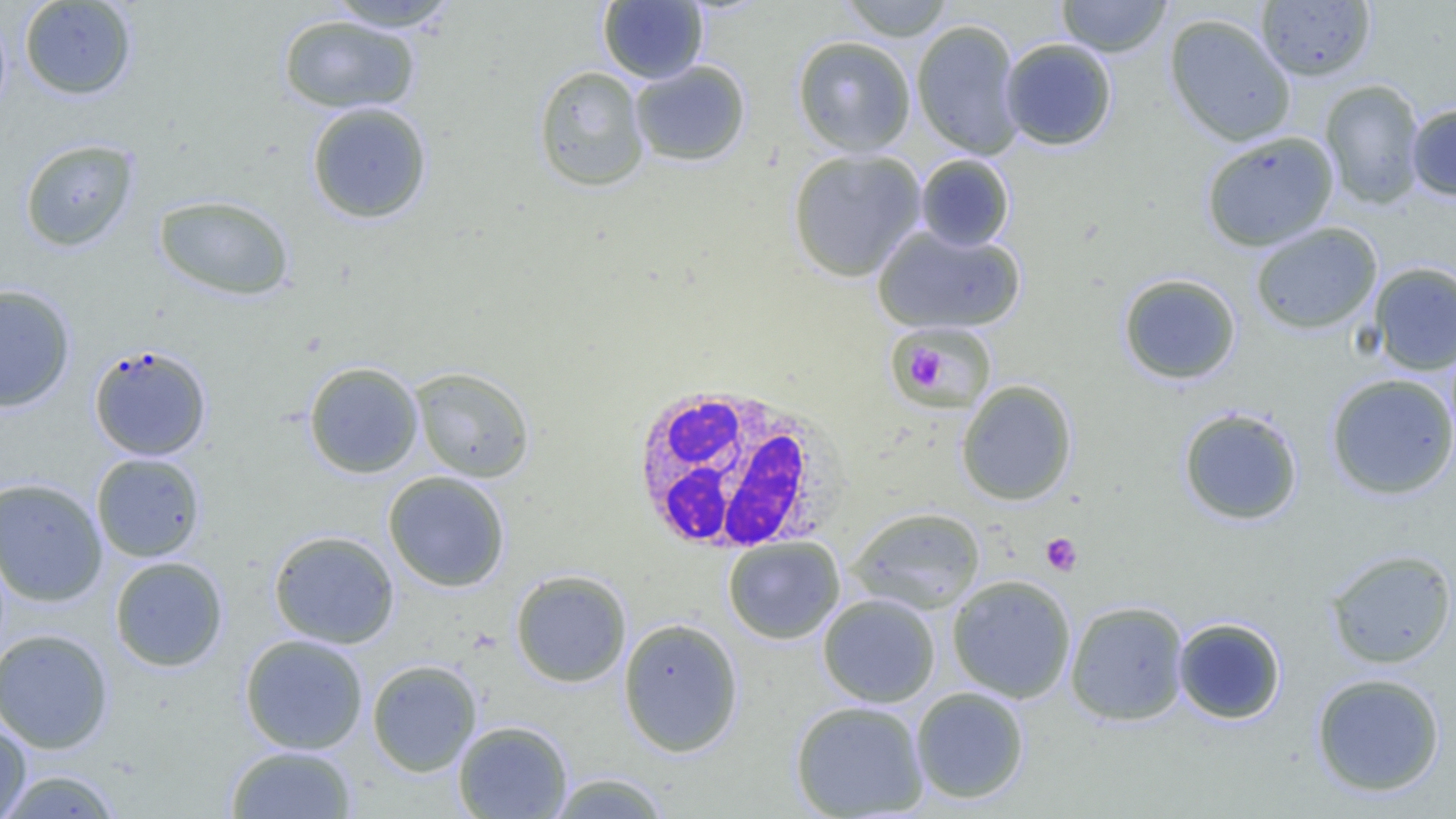

Approximate bounding boxes as [x1, y1, x2, y2] in pixels. Platelet locations: [891, 327, 988, 402], [898, 347, 949, 387], [1040, 533, 1082, 576]. Uninfected red blood cell locations: [18, 0, 137, 100], [838, 0, 956, 41], [1056, 0, 1172, 57], [1256, 0, 1376, 82], [324, 1, 463, 32], [598, 1, 708, 84], [1164, 13, 1296, 147], [277, 14, 420, 114], [911, 19, 1025, 159], [792, 36, 917, 156], [999, 38, 1117, 151], [629, 60, 751, 167], [533, 65, 650, 192], [1319, 79, 1426, 209], [306, 102, 433, 224], [1407, 104, 1456, 200], [1201, 131, 1339, 251], [19, 138, 140, 252], [786, 148, 926, 282], [914, 154, 1015, 251], [153, 194, 295, 301], [1250, 222, 1382, 335], [873, 224, 1025, 334], [1368, 262, 1456, 375], [1118, 273, 1242, 385], [0, 284, 76, 412], [893, 323, 995, 411], [304, 361, 424, 478], [410, 366, 536, 483], [1325, 373, 1456, 500], [956, 379, 1077, 506], [1177, 408, 1303, 525], [91, 452, 206, 562], [383, 471, 510, 592], [0, 477, 107, 606], [847, 507, 986, 614], [268, 530, 400, 649], [723, 536, 845, 644], [1324, 548, 1456, 669], [109, 556, 228, 672], [510, 569, 632, 687], [947, 574, 1077, 703], [817, 594, 940, 707], [1065, 600, 1189, 726], [1173, 617, 1286, 724], [618, 618, 744, 757], [0, 628, 114, 753], [239, 634, 369, 754], [366, 659, 482, 777], [1311, 672, 1446, 797], [911, 687, 1030, 804], [790, 699, 929, 818], [0, 718, 32, 819], [453, 720, 572, 818], [226, 745, 357, 818], [0, 769, 125, 818], [547, 772, 670, 818]. Plasmodium falciparum-infected red blood cell locations: [88, 343, 212, 461]. White blood cell locations: [624, 381, 849, 554]. Slide-level diagnosis: Plasmodium falciparum. Captured at 1000x magnification. Image is 1456×819 pixels. Light microscopy. One field of a larger specimen. Thin blood film.